Point out each Plasmodium parasite.
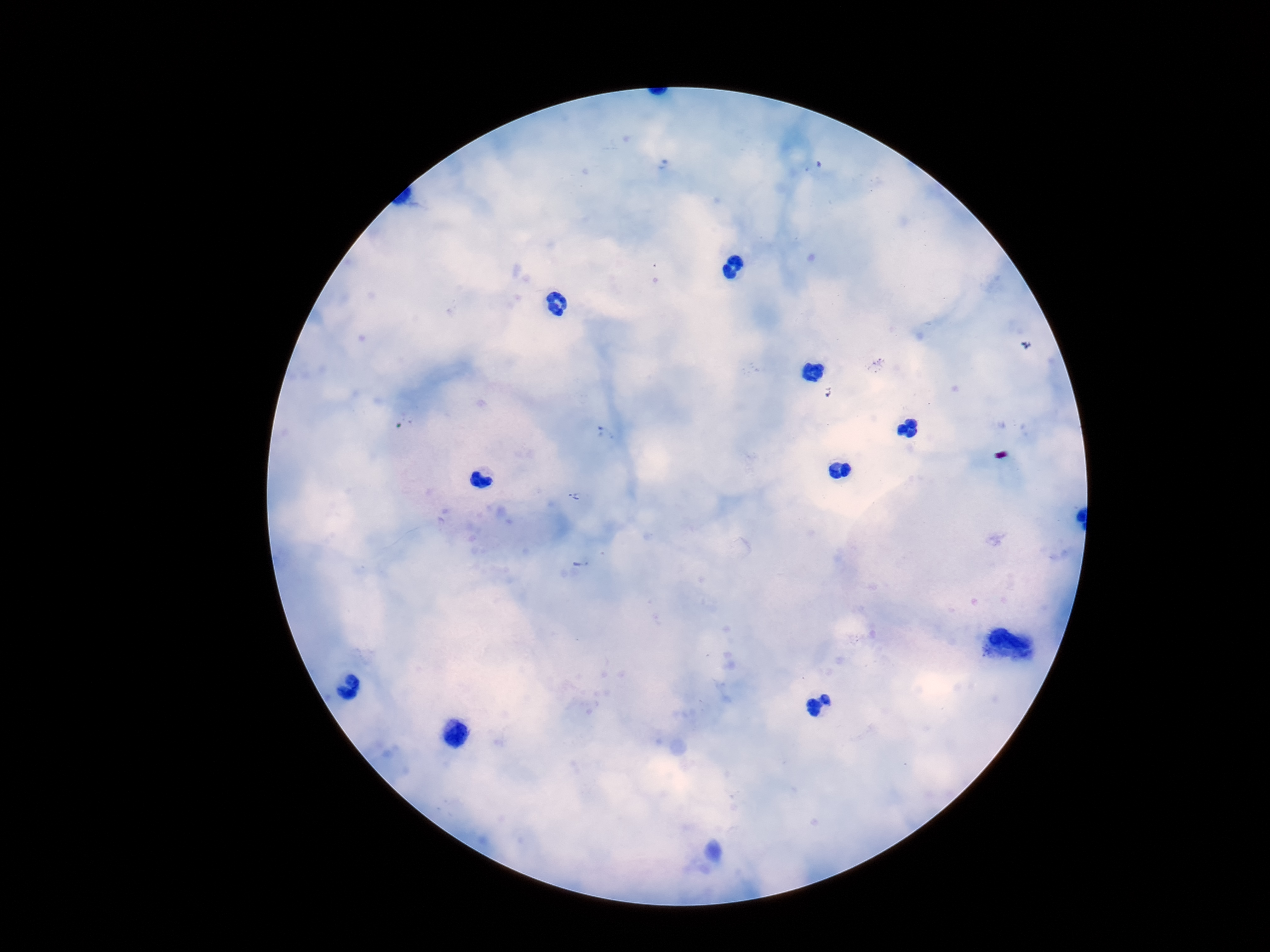

Approximate centers as [x, y] in pixels.
Plasmodium parasites: [576, 497], [582, 563].

100x magnification. One field from this slide. Patient malaria status: positive. Giemsa-stained preparation. Photographed through the microscope eyepiece with a smartphone camera. Image is 1270×952 pixels. Thick peripheral-blood smear.